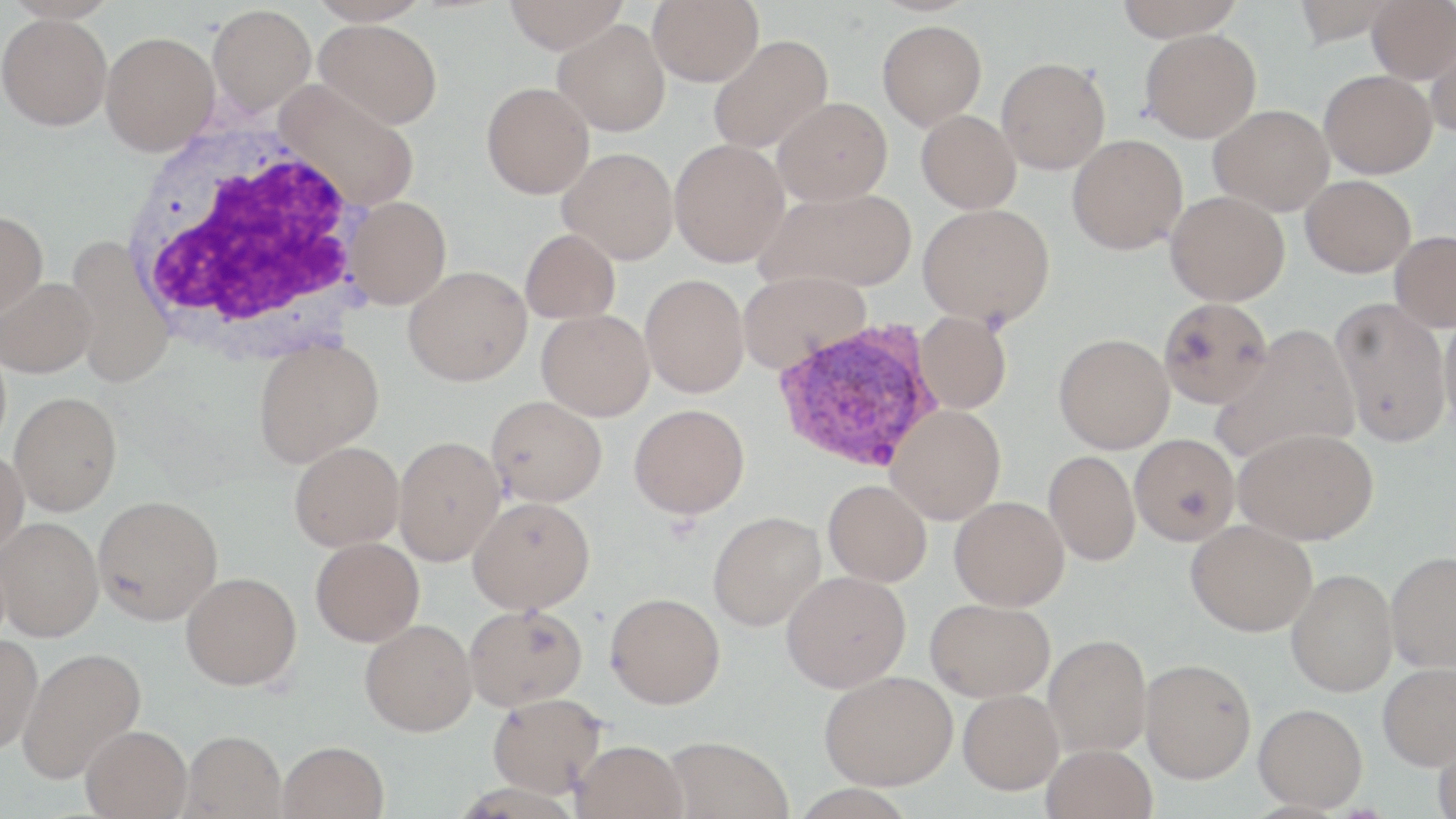

Approximate bounding boxes as (x1,y1)-(x2,y2) corner pairs in pixels. White blood cell locations: (118,119)-(373,349). Plasmodium vivax-infected red blood cell locations: (770,319)-(944,473). Uninfected red blood cell locations: (308,0)-(431,25), (504,0)-(629,54), (647,0)-(763,86), (1114,0)-(1246,41), (1366,0)-(1456,83), (208,4)-(316,116), (0,13)-(112,130), (314,19)-(443,128), (553,19)-(671,136), (878,19)-(987,130), (1140,28)-(1261,143), (1427,30)-(1456,134), (101,31)-(219,155), (707,34)-(834,155), (995,56)-(1110,174), (1319,69)-(1437,179), (275,81)-(421,210), (481,82)-(594,199), (773,97)-(892,205), (1208,104)-(1334,215), (916,109)-(1021,214), (1067,134)-(1188,254), (669,139)-(790,267), (557,147)-(678,264), (1301,175)-(1416,277), (758,187)-(916,293), (1165,190)-(1290,306), (345,196)-(451,309), (918,203)-(1055,328), (0,210)-(48,319), (520,229)-(621,324), (1389,230)-(1456,332), (66,235)-(174,389), (404,266)-(532,386), (737,270)-(870,372), (640,274)-(749,398), (1,277)-(97,377), (1157,296)-(1273,408), (1330,297)-(1452,447), (537,309)-(654,421), (1438,310)-(1456,432), (914,311)-(1012,414), (1211,324)-(1361,464), (1054,333)-(1174,454), (254,338)-(384,467), (10,392)-(122,515), (486,396)-(607,507), (629,404)-(750,519), (886,404)-(1006,524), (1234,426)-(1378,545), (1129,433)-(1240,545), (393,435)-(506,566), (289,441)-(404,551), (0,450)-(28,558), (1044,450)-(1141,566), (823,479)-(932,587), (93,495)-(223,625), (949,495)-(1069,610), (468,497)-(595,613), (708,510)-(826,631), (0,516)-(104,641), (1186,519)-(1317,636), (311,537)-(424,646), (1385,551)-(1456,672), (1286,569)-(1398,698), (781,570)-(911,693), (181,571)-(302,691), (605,592)-(725,709), (925,598)-(1055,701), (464,603)-(587,711), (360,619)-(477,736), (1044,633)-(1152,757), (0,634)-(42,752), (18,645)-(146,783), (1140,658)-(1256,783), (1378,662)-(1456,771), (819,670)-(957,790), (958,689)-(1064,794), (487,692)-(606,797), (1253,703)-(1368,812), (81,725)-(192,818), (181,730)-(286,819), (1432,732)-(1456,818), (662,735)-(794,819), (570,739)-(688,819), (277,740)-(388,819), (1041,743)-(1157,819). Slide-level diagnosis: Plasmodium vivax. Light microscopy. May-Grünwald-Giemsa-stained preparation. Captured at 1000x magnification. Thin blood smear. One field of a larger specimen. Image is 1456×819 pixels.